Name the parasite shown.
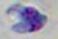
Toxoplasma gondii.

{
  "modality": "micrograph",
  "magnification": "1000x"
}